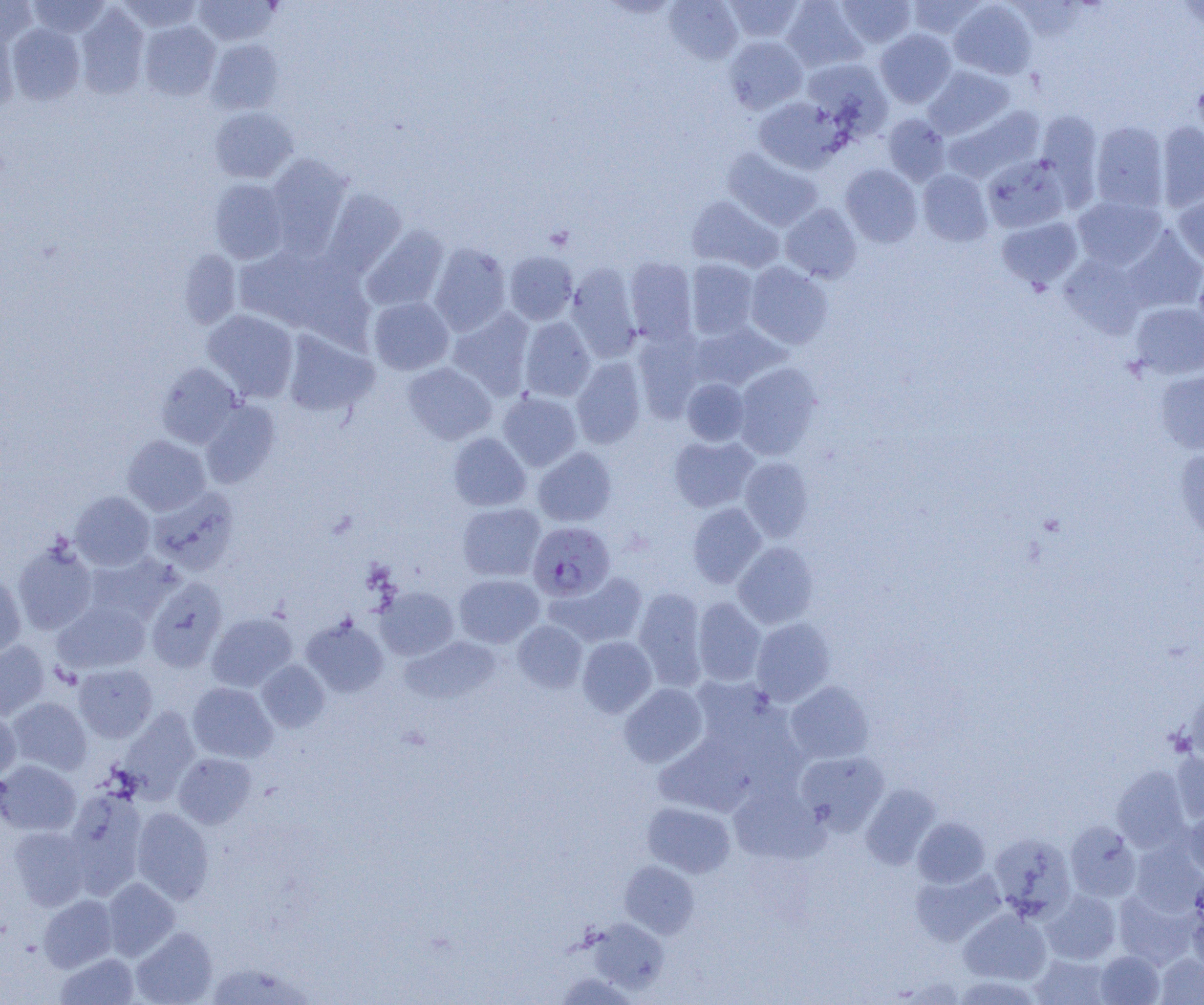
slide-level diagnosis = Plasmodium falciparum
preparation = thin blood smear
magnification = 1000x
field of view = one of a larger specimen
modality = light microscopy
Plasmodium falciparum-infected red blood cell locations = approximate bounding boxes as named x1/y1/x2/y2 corners in pixels: (x1=528, y1=522, x2=614, y2=601)
uninfected red blood cell locations = approximate bounding boxes as named x1/y1/x2/y2 corners in pixels: (x1=0, y1=0, x2=38, y2=47), (x1=28, y1=0, x2=110, y2=38), (x1=117, y1=0, x2=203, y2=33), (x1=193, y1=0, x2=278, y2=46), (x1=664, y1=0, x2=743, y2=64), (x1=724, y1=0, x2=804, y2=43), (x1=781, y1=0, x2=867, y2=72), (x1=835, y1=0, x2=916, y2=48), (x1=906, y1=0, x2=986, y2=39), (x1=949, y1=1, x2=1037, y2=80), (x1=75, y1=4, x2=150, y2=99), (x1=139, y1=20, x2=221, y2=100), (x1=0, y1=23, x2=20, y2=115), (x1=7, y1=23, x2=85, y2=104), (x1=875, y1=29, x2=956, y2=107), (x1=724, y1=35, x2=808, y2=113), (x1=207, y1=39, x2=284, y2=115), (x1=802, y1=58, x2=892, y2=136), (x1=924, y1=66, x2=1013, y2=139), (x1=1193, y1=75, x2=1204, y2=149), (x1=754, y1=97, x2=843, y2=173), (x1=944, y1=105, x2=1044, y2=182), (x1=209, y1=107, x2=298, y2=183), (x1=1036, y1=111, x2=1103, y2=203), (x1=882, y1=114, x2=950, y2=186), (x1=1090, y1=121, x2=1169, y2=212), (x1=1156, y1=122, x2=1204, y2=211), (x1=722, y1=148, x2=821, y2=231), (x1=266, y1=154, x2=352, y2=253), (x1=981, y1=155, x2=1071, y2=233), (x1=840, y1=164, x2=922, y2=247), (x1=918, y1=169, x2=993, y2=246), (x1=209, y1=179, x2=289, y2=264), (x1=323, y1=189, x2=406, y2=276), (x1=1174, y1=191, x2=1204, y2=267), (x1=1072, y1=195, x2=1166, y2=270), (x1=687, y1=196, x2=783, y2=272), (x1=781, y1=203, x2=862, y2=283), (x1=996, y1=216, x2=1083, y2=292), (x1=361, y1=225, x2=450, y2=312), (x1=1122, y1=228, x2=1204, y2=314), (x1=429, y1=243, x2=511, y2=336), (x1=234, y1=244, x2=350, y2=333), (x1=177, y1=249, x2=242, y2=329), (x1=504, y1=251, x2=577, y2=324), (x1=1059, y1=254, x2=1148, y2=337), (x1=625, y1=257, x2=697, y2=344), (x1=686, y1=259, x2=758, y2=339), (x1=745, y1=262, x2=833, y2=349), (x1=1193, y1=263, x2=1204, y2=339), (x1=566, y1=264, x2=641, y2=362), (x1=368, y1=297, x2=453, y2=375), (x1=1130, y1=301, x2=1204, y2=379), (x1=448, y1=308, x2=534, y2=398), (x1=202, y1=310, x2=299, y2=402), (x1=520, y1=316, x2=595, y2=401), (x1=690, y1=321, x2=787, y2=391), (x1=282, y1=330, x2=378, y2=417), (x1=633, y1=330, x2=706, y2=420), (x1=571, y1=357, x2=647, y2=448), (x1=155, y1=362, x2=242, y2=448), (x1=403, y1=362, x2=496, y2=444), (x1=733, y1=362, x2=823, y2=459), (x1=1155, y1=370, x2=1204, y2=455), (x1=681, y1=378, x2=750, y2=446), (x1=498, y1=392, x2=582, y2=471), (x1=200, y1=400, x2=280, y2=488), (x1=448, y1=432, x2=531, y2=511), (x1=123, y1=435, x2=211, y2=515), (x1=669, y1=435, x2=759, y2=512), (x1=533, y1=447, x2=617, y2=526), (x1=1174, y1=447, x2=1204, y2=542), (x1=739, y1=457, x2=814, y2=542), (x1=148, y1=486, x2=240, y2=575), (x1=70, y1=491, x2=155, y2=571), (x1=457, y1=503, x2=545, y2=581), (x1=687, y1=503, x2=767, y2=588), (x1=12, y1=540, x2=98, y2=635), (x1=733, y1=541, x2=819, y2=629), (x1=83, y1=553, x2=179, y2=627), (x1=550, y1=571, x2=648, y2=647), (x1=0, y1=574, x2=26, y2=659), (x1=454, y1=574, x2=544, y2=647), (x1=146, y1=577, x2=227, y2=671), (x1=377, y1=586, x2=459, y2=660), (x1=633, y1=587, x2=707, y2=689), (x1=692, y1=598, x2=766, y2=686), (x1=53, y1=600, x2=151, y2=674), (x1=207, y1=612, x2=297, y2=692), (x1=301, y1=617, x2=389, y2=697), (x1=750, y1=618, x2=835, y2=705), (x1=513, y1=620, x2=587, y2=692), (x1=400, y1=636, x2=501, y2=705), (x1=577, y1=636, x2=657, y2=717), (x1=0, y1=641, x2=49, y2=720), (x1=257, y1=660, x2=330, y2=732), (x1=74, y1=664, x2=157, y2=742), (x1=785, y1=681, x2=874, y2=764), (x1=1183, y1=681, x2=1204, y2=765), (x1=187, y1=682, x2=277, y2=762), (x1=619, y1=683, x2=708, y2=768), (x1=7, y1=697, x2=91, y2=775), (x1=117, y1=707, x2=199, y2=801), (x1=0, y1=709, x2=21, y2=782), (x1=794, y1=750, x2=889, y2=835), (x1=1170, y1=751, x2=1204, y2=825), (x1=173, y1=753, x2=257, y2=828), (x1=0, y1=759, x2=81, y2=836), (x1=1112, y1=765, x2=1191, y2=852), (x1=728, y1=783, x2=826, y2=864), (x1=860, y1=784, x2=939, y2=870), (x1=65, y1=789, x2=147, y2=896), (x1=642, y1=801, x2=735, y2=877), (x1=131, y1=807, x2=214, y2=903), (x1=1183, y1=809, x2=1204, y2=878), (x1=912, y1=817, x2=990, y2=888), (x1=1065, y1=821, x2=1141, y2=902), (x1=9, y1=826, x2=90, y2=910), (x1=988, y1=832, x2=1076, y2=920), (x1=1129, y1=841, x2=1204, y2=915), (x1=620, y1=860, x2=699, y2=938), (x1=911, y1=868, x2=1005, y2=946), (x1=102, y1=877, x2=180, y2=960), (x1=1041, y1=890, x2=1121, y2=965), (x1=1113, y1=890, x2=1197, y2=969), (x1=38, y1=895, x2=117, y2=972), (x1=1185, y1=898, x2=1204, y2=973), (x1=959, y1=908, x2=1051, y2=984), (x1=589, y1=919, x2=669, y2=993), (x1=131, y1=927, x2=217, y2=1005), (x1=1094, y1=950, x2=1165, y2=1005), (x1=56, y1=952, x2=139, y2=1005), (x1=1155, y1=953, x2=1204, y2=1004), (x1=1030, y1=955, x2=1113, y2=1005), (x1=206, y1=962, x2=314, y2=1004), (x1=555, y1=972, x2=637, y2=1004), (x1=952, y1=975, x2=1043, y2=1004)
image size = 1204×1005 pixels